Report the malaria status of this cell.
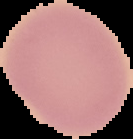

It is uninfected.

From a thin blood smear. The area outside the segmented cell region is set to black. Image is 133×139 pixels.